Assess the morphology of the erythrocytes.
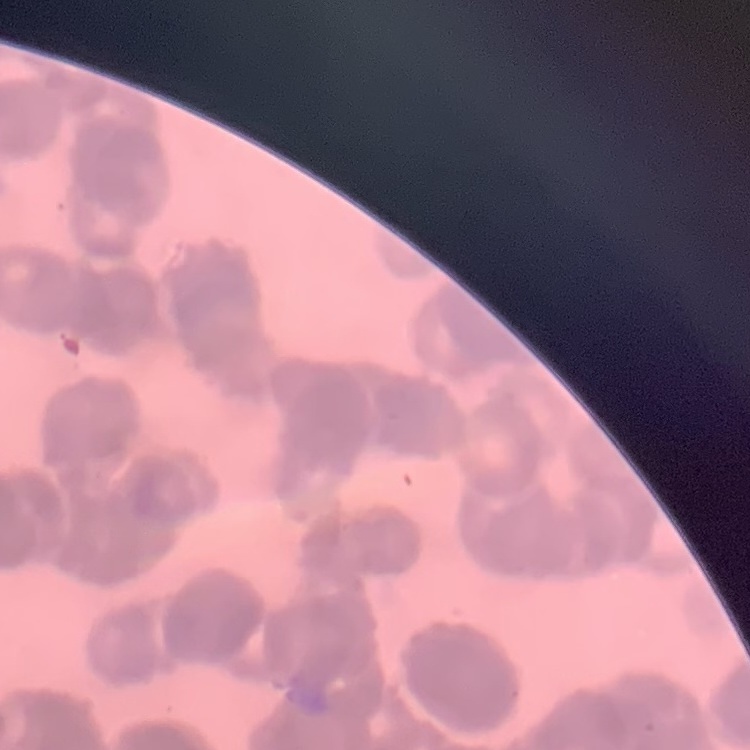
Rouleaux formation.

Summary:
  - Preparation: thin peripheral smear
  - Stain: Field's or Giemsa
  - Image type: one tile cut from a larger photomicrograph